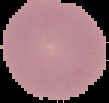
The area outside the segmented cell region is set to black. From a thin blood film. Malaria status: uninfected. Image is 109×103 pixels.